Classify this cell by malaria status.
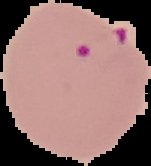
It is parasitized.

image size = 151×166 pixels
preparation = thin blood film
image type = segmented cell region on a black background